Classify this cell by malaria status.
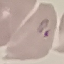

It is parasitized.

stain: Giemsa
preparation: thin smear
image_type: automatically extracted cell patch, resized to 64 × 64 pixels
capture: smartphone camera at the microscope eyepiece